Assess this cell for malaria.
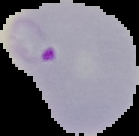
It is parasitized.

From a thin blood smear. Segmented cell region on a black background. Image is 139×136 pixels.